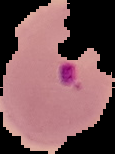

Result: malaria parasites detected. Cell region segmented out of the field of view; the surrounding area is masked to black. From a thin blood film. Image is 115×154 pixels.